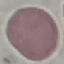
result: no malaria parasites seen
stain: Giemsa
image_type: cell patch, automatically extracted from a larger field of view and resized to 64 × 64 pixels
preparation: thin blood film
capture: smartphone through the microscope eyepiece